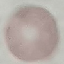

Summary:
  - Result: no malaria parasites seen
  - Preparation: thin blood smear
  - Stain: Giemsa
  - Capture: smartphone through the microscope eyepiece
  - Image type: automatically extracted cell patch, resized to 64 × 64 pixels